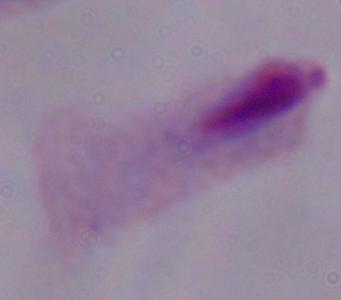
Summary:
  - Magnification: 1000x
  - Modality: photomicrograph
  - Identification: trichomonad